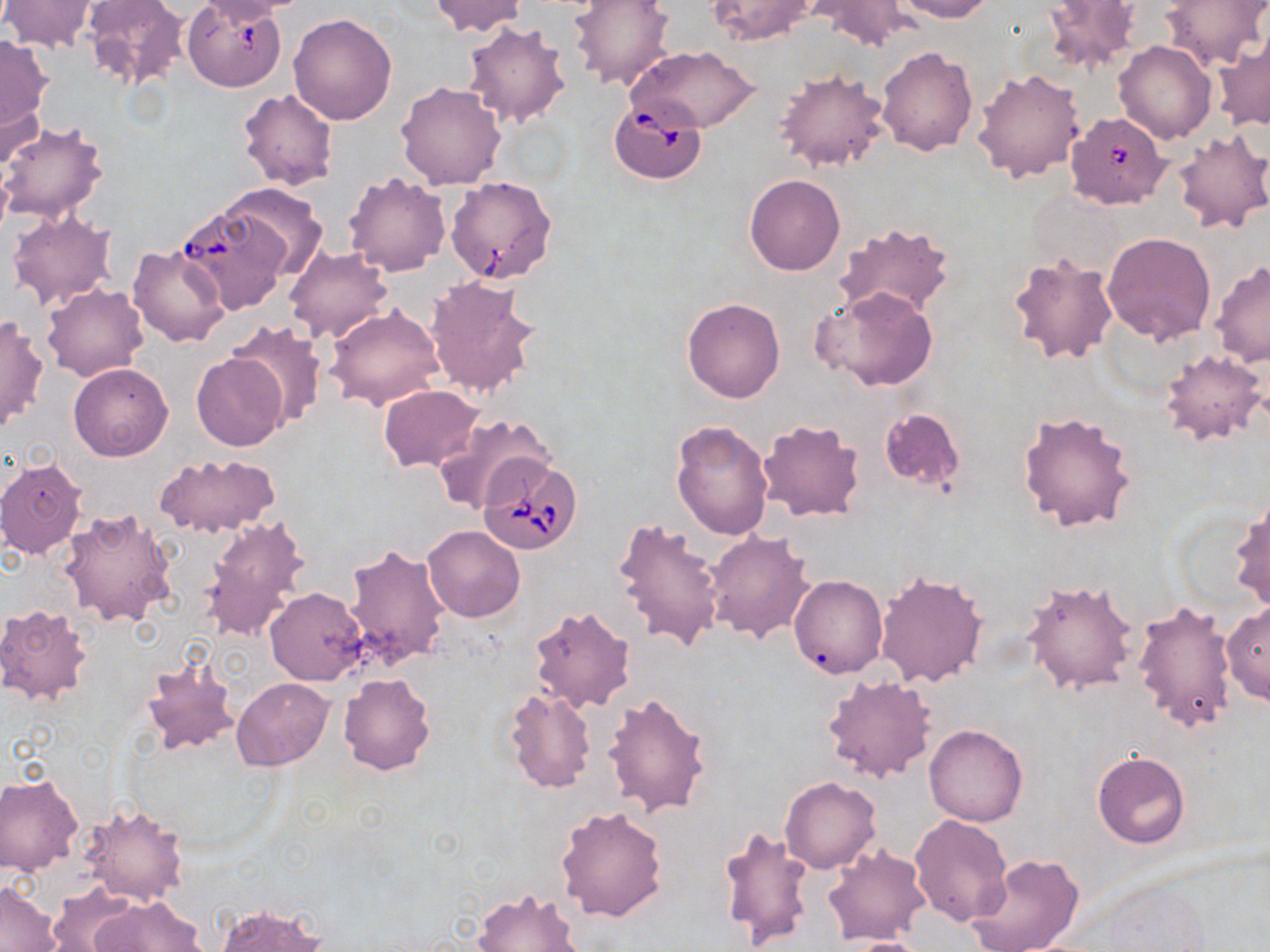 Approximate bounding boxes as (x1, y1, x2, y2) in pixels. Uninfected red blood cell locations: (83, 0, 188, 91), (193, 0, 302, 24), (429, 0, 528, 35), (569, 0, 677, 90), (806, 0, 922, 51), (891, 0, 996, 22), (1044, 0, 1142, 72), (1159, 0, 1267, 71), (1, 1, 99, 52), (707, 1, 820, 45), (289, 13, 397, 124), (461, 20, 572, 128), (0, 34, 54, 133), (1213, 35, 1270, 131), (1114, 40, 1217, 143), (629, 45, 760, 133), (877, 46, 979, 156), (774, 67, 892, 174), (972, 68, 1086, 183), (396, 81, 507, 190), (0, 86, 45, 178), (237, 88, 339, 191), (0, 120, 111, 224), (1170, 128, 1270, 236), (343, 171, 451, 275), (744, 174, 845, 276), (218, 182, 328, 281), (174, 201, 288, 315), (7, 209, 117, 313), (834, 221, 954, 320), (1102, 231, 1216, 343), (127, 245, 231, 348), (284, 246, 394, 343), (1006, 251, 1119, 366), (1209, 259, 1270, 367), (425, 275, 542, 402), (42, 283, 147, 381), (813, 288, 939, 391), (682, 298, 785, 403), (325, 305, 446, 411), (1, 315, 48, 434), (226, 320, 328, 426), (1159, 349, 1267, 444), (192, 353, 289, 451), (68, 363, 173, 462), (377, 385, 484, 471), (878, 406, 966, 493), (1016, 409, 1137, 533), (433, 412, 552, 514), (756, 419, 866, 522), (670, 421, 773, 540), (153, 451, 281, 539), (0, 457, 88, 558), (1229, 495, 1269, 613), (59, 507, 177, 628), (200, 514, 312, 642), (610, 516, 725, 653), (422, 525, 525, 623), (705, 529, 814, 643), (343, 543, 452, 668), (874, 569, 988, 687), (789, 575, 887, 678), (1020, 580, 1138, 696), (265, 587, 367, 686), (1132, 597, 1237, 736), (1221, 603, 1270, 707), (0, 605, 92, 707), (528, 605, 636, 713), (140, 654, 241, 758), (338, 673, 436, 774), (821, 674, 937, 783), (231, 677, 332, 771), (502, 687, 596, 793), (603, 692, 714, 819), (924, 723, 1028, 826), (1092, 752, 1189, 848), (0, 775, 83, 875), (781, 776, 881, 874), (79, 802, 190, 904), (555, 804, 669, 923), (910, 814, 1013, 925), (718, 823, 817, 949), (821, 844, 932, 945), (967, 853, 1085, 952), (1104, 877, 1209, 951), (0, 881, 60, 951), (48, 884, 140, 952), (472, 887, 585, 952), (92, 895, 206, 952), (214, 902, 329, 952), (838, 936, 938, 951). Babesia divergens-infected red blood cell locations: (182, 1, 288, 92), (609, 99, 707, 183), (1065, 111, 1171, 209), (446, 176, 557, 283), (480, 455, 585, 556). Slide-level diagnosis: Babesia divergens. Thin blood film. Optical microscopy. One field of a larger specimen. Image is 1270×952 pixels. May-Grünwald-Giemsa stain. 1000x magnification.